State which cell type is depicted.
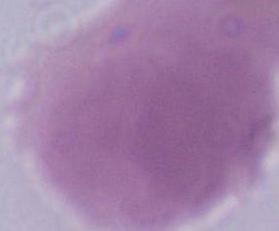

An erythrocyte.

Micrograph. Captured at 1000x magnification.